Name the parasite shown.
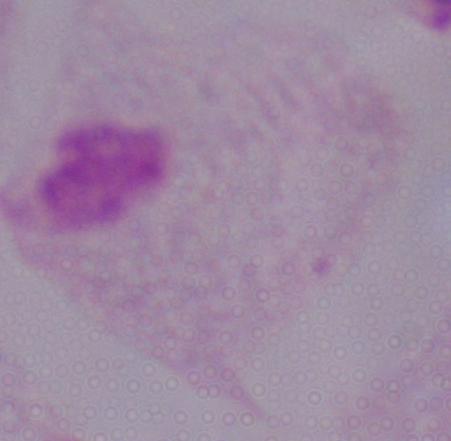
A trichomonad.

{
  "modality": "photomicrograph",
  "magnification": "1000x"
}